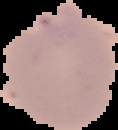
{
  "preparation": "thin blood smear",
  "image_type": "cell region segmented out of the field of view; surrounding area masked to black",
  "image_size": "118×130 pixels",
  "result": "malaria parasites detected"
}